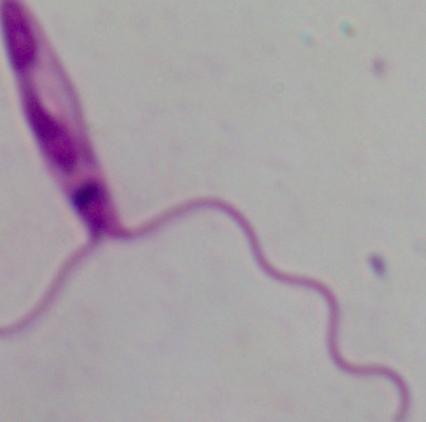

Photomicrograph. A Leishmania parasite is seen. Captured at 1000x magnification.